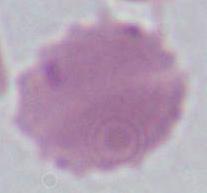

Micrograph. 1000x magnification. An erythrocyte is seen.